Give the extent of all uninfected red blood cells.
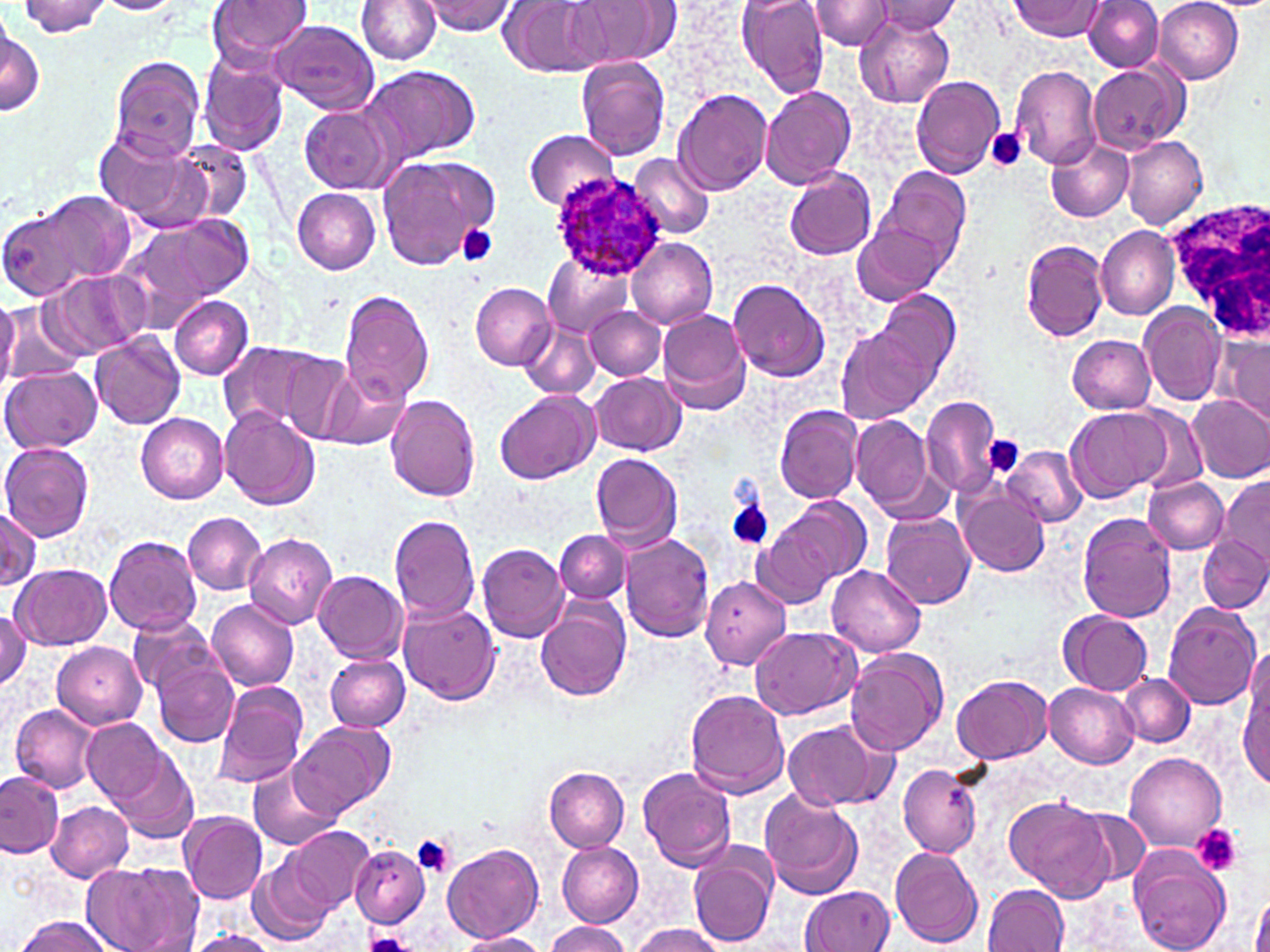
Approximate bounding boxes as (x1, y1, x2, y2) in pixels.
Uninfected red blood cells: (94, 0, 181, 15), (208, 0, 315, 66), (357, 0, 442, 64), (423, 0, 516, 34), (499, 0, 607, 77), (567, 0, 675, 67), (738, 0, 830, 97), (809, 0, 894, 51), (1154, 0, 1244, 84), (19, 1, 114, 37), (1010, 1, 1105, 39), (1082, 1, 1163, 72), (875, 3, 960, 39), (855, 13, 955, 108), (0, 16, 44, 119), (269, 20, 380, 116), (199, 54, 291, 156), (109, 56, 205, 162), (576, 56, 671, 160), (1089, 63, 1183, 153), (363, 65, 480, 166), (1008, 65, 1102, 169), (910, 74, 1005, 180), (760, 86, 857, 189), (674, 88, 773, 195), (298, 104, 399, 195), (92, 128, 208, 230), (524, 128, 620, 209), (1122, 136, 1208, 228), (172, 138, 252, 223), (1046, 140, 1135, 222), (629, 152, 716, 240), (375, 154, 497, 272), (875, 165, 970, 267), (784, 167, 877, 261), (293, 188, 382, 274), (33, 189, 136, 289), (1, 206, 94, 302), (118, 213, 253, 325), (853, 224, 947, 306), (1096, 225, 1180, 321), (626, 234, 718, 330), (1020, 240, 1110, 342), (542, 252, 636, 338), (45, 269, 151, 358), (728, 278, 830, 383), (470, 282, 557, 369), (876, 288, 960, 381), (340, 290, 435, 405), (170, 296, 253, 380), (0, 297, 21, 390), (2, 304, 82, 386), (1140, 304, 1228, 406), (585, 306, 665, 380), (658, 310, 754, 414), (519, 321, 602, 401), (838, 328, 934, 423), (90, 331, 184, 430), (1223, 333, 1269, 428), (1067, 334, 1156, 415), (218, 342, 327, 433), (282, 354, 358, 443), (0, 365, 101, 454), (322, 367, 410, 450), (592, 373, 688, 456), (495, 391, 599, 484), (386, 393, 481, 501), (1188, 393, 1270, 483), (920, 395, 1000, 499), (775, 404, 864, 503), (1066, 407, 1171, 502), (869, 408, 991, 513), (1131, 408, 1205, 493), (220, 409, 320, 511), (135, 412, 228, 504), (850, 414, 935, 516), (0, 443, 93, 540), (1003, 445, 1086, 527), (591, 452, 684, 552), (1144, 476, 1229, 553), (1217, 476, 1270, 570), (955, 483, 1052, 578), (767, 497, 870, 597), (0, 508, 41, 592), (183, 511, 268, 594), (881, 512, 976, 608), (1076, 512, 1178, 622), (388, 514, 481, 622), (754, 522, 839, 608), (554, 531, 630, 603), (621, 532, 716, 641), (244, 533, 338, 629), (104, 535, 202, 636), (1198, 536, 1270, 614), (475, 543, 571, 643), (12, 565, 112, 651), (828, 565, 926, 657), (314, 570, 407, 662), (700, 575, 792, 671), (533, 598, 631, 702), (206, 599, 299, 692), (398, 602, 502, 706), (1163, 602, 1261, 709), (0, 606, 30, 692), (1059, 610, 1154, 695), (126, 613, 217, 698), (751, 627, 859, 719), (53, 641, 147, 730), (846, 647, 949, 756), (1243, 647, 1270, 741), (325, 654, 411, 732), (151, 655, 240, 747), (1118, 673, 1194, 746), (952, 674, 1052, 764), (1238, 680, 1269, 790), (212, 682, 310, 790), (1045, 682, 1139, 767), (686, 690, 791, 797), (11, 704, 101, 793), (84, 719, 164, 801), (783, 719, 889, 814), (290, 722, 393, 819), (113, 751, 198, 843), (1125, 753, 1227, 851), (898, 763, 983, 858), (249, 764, 341, 851), (544, 767, 630, 851), (638, 768, 737, 871), (0, 770, 64, 859), (760, 790, 865, 900), (1005, 795, 1114, 903), (47, 801, 132, 882), (1074, 806, 1153, 888), (180, 810, 269, 903), (289, 825, 373, 913), (556, 841, 643, 927), (349, 843, 430, 927), (441, 843, 544, 944), (1128, 845, 1233, 952), (889, 846, 986, 948), (690, 851, 777, 947), (250, 856, 336, 943), (83, 864, 200, 951), (982, 883, 1070, 952), (800, 884, 895, 952), (1252, 886, 1270, 952), (16, 916, 115, 952), (547, 921, 630, 952), (631, 924, 723, 952), (185, 929, 278, 952), (455, 931, 548, 952).

Summary:
  - Plasmodium ovale-infected red blood cell locations: (550, 173, 669, 281)
  - White blood cell locations: (1159, 194, 1270, 342)
  - Platelet locations: (986, 128, 1026, 172), (456, 223, 500, 267), (984, 436, 1024, 478), (727, 499, 774, 552), (1193, 824, 1242, 876), (411, 835, 457, 877), (364, 933, 414, 952)
  - Slide-level diagnosis: Plasmodium ovale
  - Preparation: thin blood film
  - Modality: optical microscopy
  - Field of view: one of a larger specimen
  - Stain: May-Grünwald-Giemsa
  - Magnification: 1000x
  - Image size: 1270×952 pixels